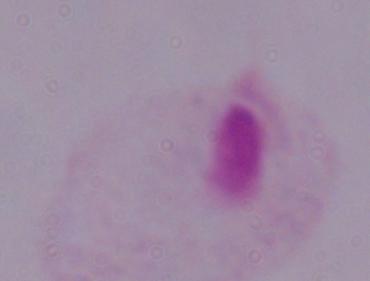
Summary:
  - Modality: photomicrograph
  - Magnification: 1000x
  - Identification: trichomonad